Outline each blood parasite and name the species.
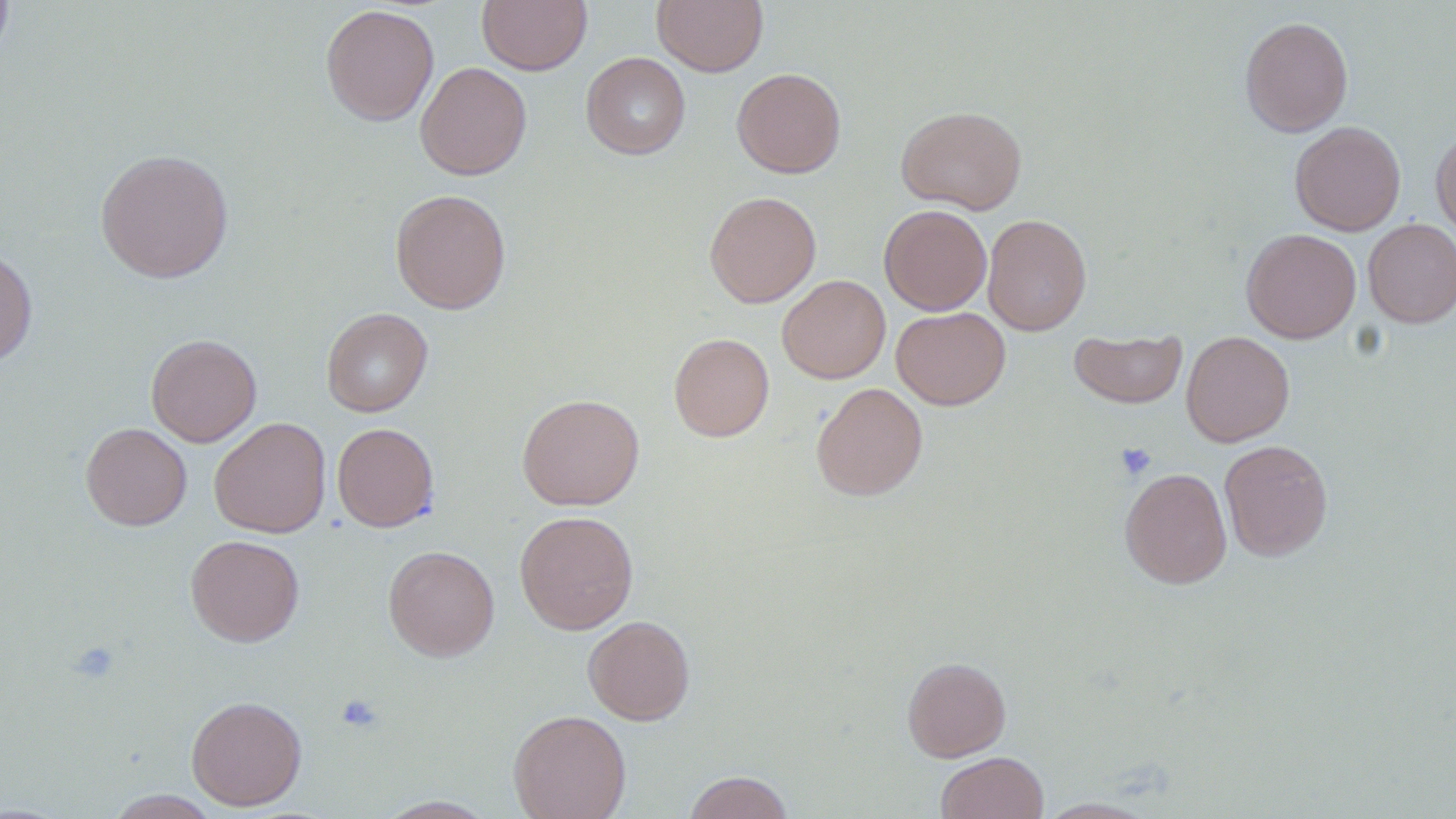

No blood parasites observed.

{
  "slide_level_diagnosis": "no evidence of blood parasites",
  "preparation": "thin blood smear",
  "magnification": "1000x",
  "uninfected_red_blood_cell_locations": "approximate bounding boxes as (x1, y1, x2, y2) in pixels: (0, 0, 14, 63), (477, 0, 592, 75), (652, 0, 768, 76), (319, 4, 439, 126), (1239, 15, 1354, 137), (581, 52, 691, 159), (415, 61, 532, 180), (731, 67, 846, 178), (896, 106, 1027, 214), (1289, 121, 1406, 235), (1431, 125, 1456, 240), (95, 148, 234, 283), (390, 189, 511, 314), (704, 191, 821, 308), (879, 204, 992, 315), (982, 214, 1091, 335), (1362, 219, 1456, 327), (1241, 228, 1360, 343), (0, 245, 38, 367), (777, 275, 890, 383), (891, 306, 1010, 410), (321, 307, 433, 417), (1069, 329, 1187, 409), (1181, 331, 1295, 447), (669, 333, 774, 442), (146, 334, 261, 447), (811, 382, 928, 501), (517, 393, 644, 511), (209, 417, 331, 538), (81, 422, 192, 530), (332, 422, 439, 532), (1219, 439, 1333, 561), (1119, 467, 1232, 588), (514, 510, 639, 635), (185, 534, 305, 647), (383, 545, 500, 661), (583, 615, 695, 725), (902, 656, 1011, 762), (186, 695, 307, 810), (508, 709, 631, 819), (936, 751, 1048, 818), (683, 770, 795, 819), (105, 790, 223, 818), (375, 795, 498, 818), (1036, 797, 1160, 818)",
  "platelet_locations": "approximate bounding boxes as (x1, y1, x2, y2) in pixels: (1115, 442, 1157, 481), (69, 641, 120, 684), (336, 694, 385, 734)",
  "field_of_view": "single",
  "stain": "May-Grünwald-Giemsa",
  "image_size": "1456×819 pixels",
  "modality": "optical microscopy"
}